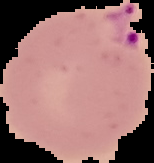

{
  "image_size": "154×163 pixels",
  "result": "Plasmodium parasites identified",
  "image_type": "segmented cell region on a black background",
  "preparation": "thin blood smear"
}